Assess this cell for malaria.
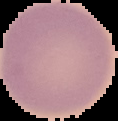

Uninfected.

The area outside the segmented cell region is set to black. From a thin blood film. Image is 118×121 pixels.